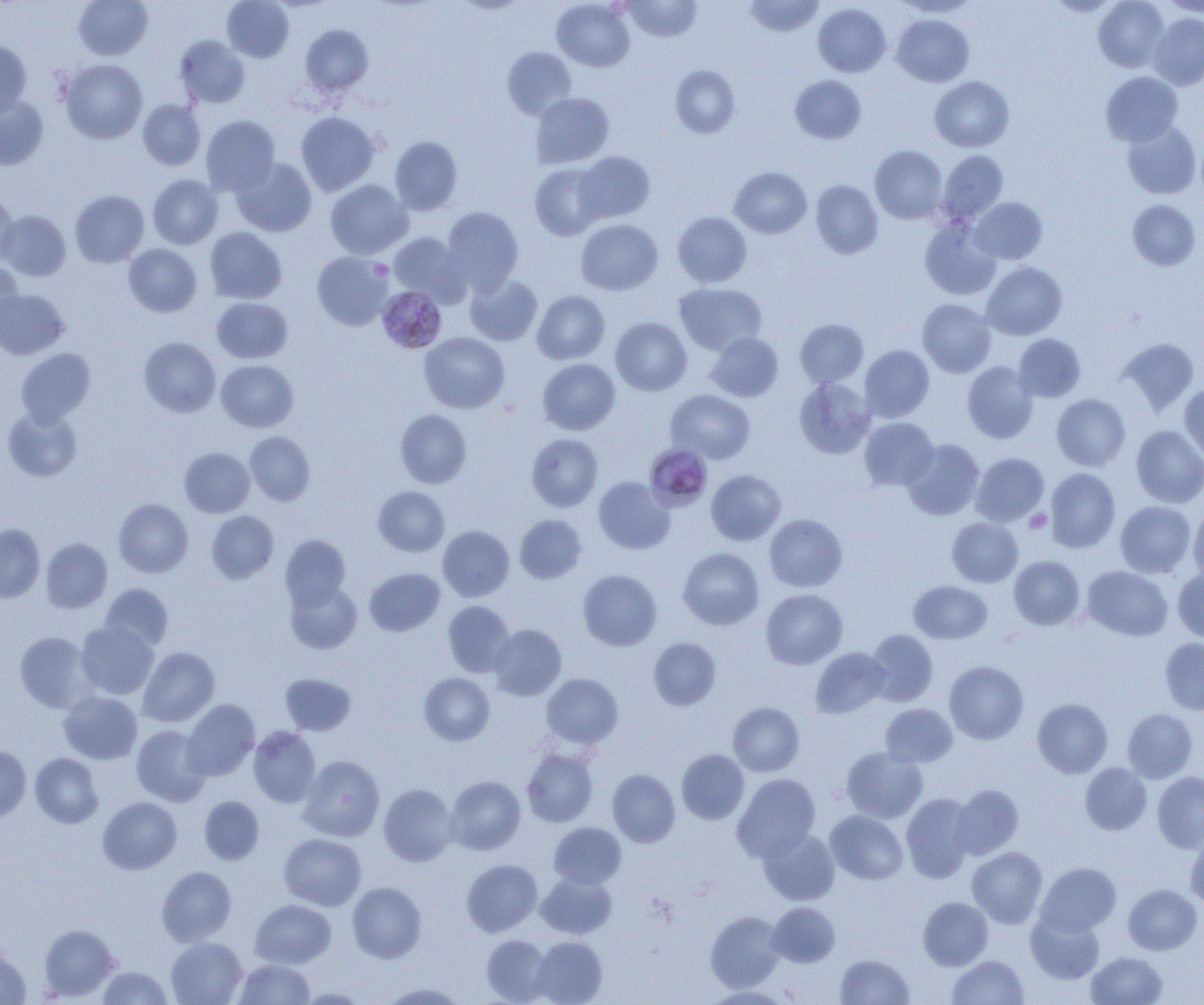
plasmodium_malariae_infected_red_blood_cell_locations: 'approximate bounding boxes as (x1,y1)-(x2,y2) corner pairs in pixels: (380,291)-(449,354), (647,451)-(712,517)'
slide_level_diagnosis: Plasmodium malariae
modality: light microscopy
image_size: 1204×1005 pixels
field_of_view: single
preparation: thin blood film
magnification: 1000x
uninfected_red_blood_cell_locations: 'approximate bounding boxes as (x1,y1)-(x2,y2) corner pairs in pixels: (73,0)-(153,60), (222,0)-(294,62), (552,0)-(635,72), (621,0)-(701,42), (744,0)-(825,37), (1093,0)-(1169,72), (1159,0)-(1204,18), (895,1)-(980,17), (813,3)-(891,77), (1148,12)-(1204,90), (891,14)-(974,87), (300,24)-(373,96), (174,35)-(250,109), (0,39)-(32,118), (502,46)-(577,120), (60,59)-(147,144), (670,64)-(740,138), (1101,71)-(1183,146), (790,75)-(866,143), (930,76)-(1014,152), (531,93)-(614,168), (0,95)-(48,170), (138,99)-(205,170), (295,111)-(380,196), (201,115)-(280,195), (1121,120)-(1201,199), (389,136)-(462,215), (869,145)-(947,224), (937,150)-(1008,224), (575,151)-(655,224), (231,157)-(316,237), (530,163)-(606,240), (730,167)-(812,238), (147,175)-(223,249), (325,179)-(413,259), (811,180)-(883,259), (70,190)-(149,267), (0,193)-(17,266), (970,197)-(1047,264), (1127,200)-(1200,270), (442,206)-(523,293), (0,210)-(71,281), (673,212)-(752,288), (576,219)-(663,296), (920,219)-(1001,301), (204,227)-(286,304), (388,233)-(469,305), (124,243)-(202,317), (312,251)-(394,330), (0,260)-(22,333), (981,262)-(1067,340), (465,274)-(542,346), (674,283)-(766,355), (0,288)-(69,360), (532,290)-(610,364), (212,297)-(293,363), (917,299)-(996,378), (610,317)-(692,396), (795,319)-(868,388), (705,331)-(783,402), (419,332)-(510,414), (1013,334)-(1086,402), (139,337)-(221,417), (1118,338)-(1199,415), (859,345)-(934,422), (16,348)-(95,425), (537,358)-(620,435), (216,359)-(299,432), (962,361)-(1039,444), (793,376)-(876,459), (1179,384)-(1204,465), (666,390)-(755,464), (1052,394)-(1131,471), (2,406)-(83,482), (395,409)-(472,488), (859,417)-(938,490), (1131,425)-(1204,507), (244,431)-(315,505), (527,434)-(603,512), (902,439)-(984,521), (179,447)-(254,517), (970,453)-(1049,526), (1045,468)-(1120,552), (706,469)-(785,545), (593,477)-(675,554), (373,486)-(449,557), (113,498)-(193,578), (1115,501)-(1196,578), (1188,504)-(1204,584), (206,510)-(279,583), (514,514)-(588,584), (764,514)-(847,592), (947,517)-(1023,587), (0,524)-(45,603), (437,525)-(514,602), (280,535)-(350,608), (41,538)-(112,613), (678,547)-(764,630), (1009,556)-(1085,630), (1082,566)-(1173,641), (364,568)-(445,637), (1173,568)-(1204,645), (578,569)-(661,651), (285,579)-(362,654), (908,581)-(992,644), (100,583)-(173,651), (761,589)-(847,669), (443,601)-(514,677), (75,621)-(159,700), (488,624)-(567,701), (864,629)-(938,707), (14,632)-(95,712), (648,637)-(721,711), (1160,637)-(1204,715), (138,647)-(220,727), (810,647)-(890,718), (944,660)-(1028,744), (279,673)-(356,736), (418,673)-(494,746), (542,673)-(623,749), (58,690)-(142,764), (1032,698)-(1113,778), (181,699)-(259,781), (728,702)-(804,777), (880,703)-(957,767), (1122,708)-(1197,783), (131,725)-(212,807), (248,726)-(321,808), (0,746)-(31,822), (841,746)-(928,823), (522,749)-(598,827), (676,749)-(749,824), (30,753)-(103,828), (299,755)-(384,841), (1080,763)-(1152,836), (607,769)-(680,847), (1152,771)-(1204,853), (732,773)-(820,862), (445,776)-(525,855), (378,783)-(458,866), (950,784)-(1023,860), (901,793)-(977,882), (198,796)-(264,865), (97,797)-(181,874), (825,810)-(908,885), (548,822)-(626,889), (758,827)-(840,905), (279,834)-(365,911), (1185,834)-(1204,910), (967,846)-(1048,928), (461,859)-(542,936), (1035,862)-(1120,936), (156,866)-(236,947), (535,872)-(617,939), (347,882)-(426,963), (1123,884)-(1202,954), (918,897)-(993,970), (251,899)-(335,968), (767,902)-(840,967), (705,910)-(785,992), (1026,910)-(1105,984), (39,924)-(119,1001), (481,934)-(553,1004), (531,936)-(607,1005), (166,937)-(247,1005), (0,951)-(31,1004), (1086,951)-(1167,1005), (835,954)-(914,1004), (947,955)-(1028,1005), (234,958)-(315,1004), (96,966)-(175,1005), (377,983)-(467,1004), (702,985)-(796,1004), (296,988)-(372,1004)'
platelet_locations: 'approximate bounding boxes as (x1,y1)-(x2,y2) corner pairs in pixels: (1024,509)-(1052,533)'